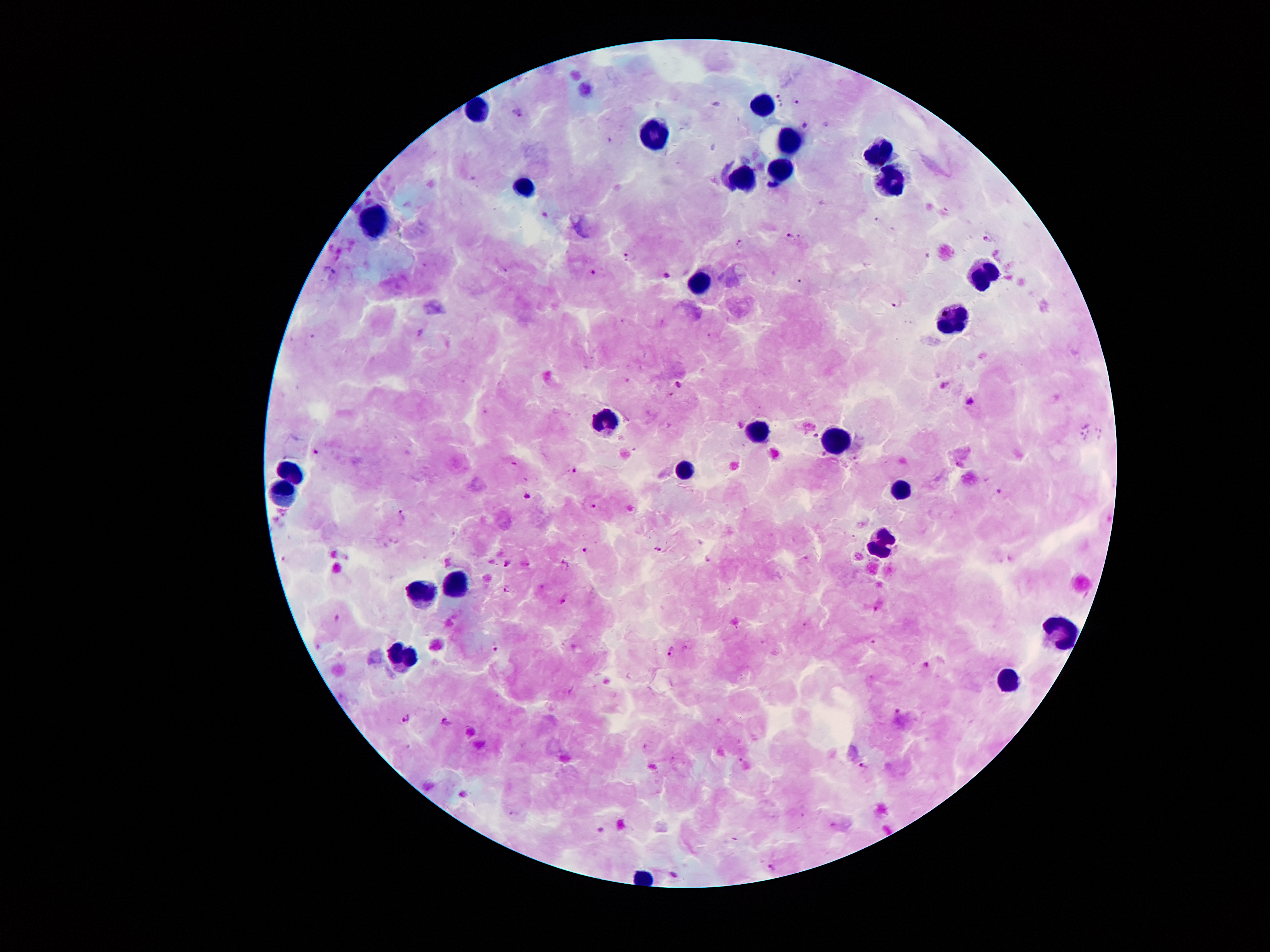
coordinate format = approximate object centers, in pixels from the top-left corner
leukocyte locations = (x=761, y=108), (x=478, y=113), (x=655, y=138), (x=787, y=144), (x=879, y=154), (x=777, y=166), (x=887, y=178), (x=741, y=182), (x=526, y=190), (x=377, y=218), (x=979, y=270), (x=701, y=285), (x=954, y=319), (x=605, y=418), (x=758, y=436), (x=839, y=442), (x=683, y=469), (x=291, y=474), (x=903, y=490), (x=282, y=494), (x=882, y=541), (x=455, y=588), (x=425, y=593), (x=1059, y=631), (x=402, y=652), (x=1010, y=679)
Plasmodium parasite locations = (x=781, y=102), (x=798, y=102), (x=519, y=114), (x=805, y=124), (x=545, y=212), (x=790, y=236), (x=987, y=238), (x=741, y=243), (x=629, y=254), (x=329, y=272), (x=595, y=272), (x=668, y=274), (x=897, y=304), (x=678, y=384), (x=945, y=385), (x=970, y=401), (x=816, y=435), (x=315, y=452), (x=515, y=467), (x=574, y=469), (x=1000, y=492), (x=528, y=495), (x=593, y=506), (x=401, y=516), (x=657, y=549), (x=586, y=550), (x=709, y=559), (x=508, y=562), (x=565, y=565), (x=508, y=590), (x=563, y=601), (x=496, y=649), (x=671, y=651), (x=925, y=663), (x=898, y=709), (x=408, y=719), (x=446, y=723), (x=864, y=766), (x=463, y=794), (x=771, y=868), (x=677, y=875)
patient malaria status = positive for Plasmodium falciparum
image size = 1270×952 pixels
capture = smartphone through the microscope eyepiece
stain = Giemsa
magnification = 100x
field of view = single
preparation = thick peripheral-blood smear